Assess this cell for malaria.
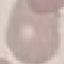
Uninfected.

Giemsa stain. Thin blood film. Acquired by smartphone through the microscope eyepiece. Cell patch, automatically extracted from a larger field of view and resized to 64 × 64 pixels.